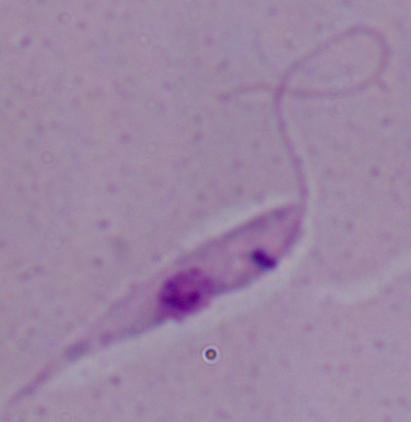

Summary:
  - Magnification: 1000x
  - Modality: photomicrograph
  - Identification: Leishmania